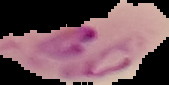

Image is 169×85 pixels. From a thin blood film. Malaria status: parasitized. Cell region segmented out of the field of view; the surrounding area is masked to black.